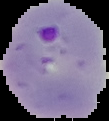 From a thin blood smear. Segmented cell region on a black background. Malaria status: parasitized. Image is 109×121 pixels.